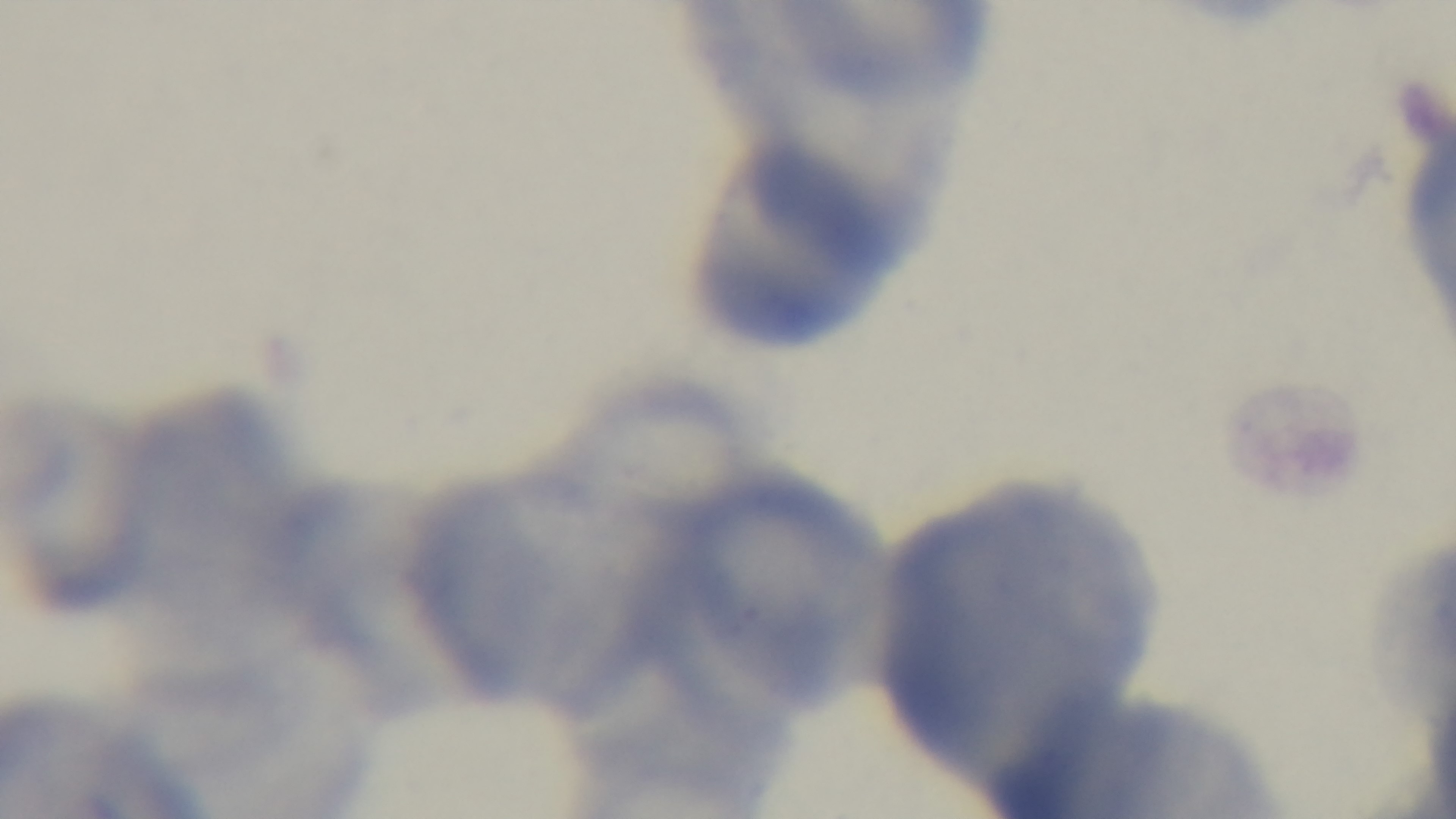
capture = mounted 4K digital camera
modality = light microscopy
objective = 100x oil immersion
stain = Giemsa
malaria status = negative
preparation = thin
field of view = one from the slide